Assess the morphology of the red blood cells.
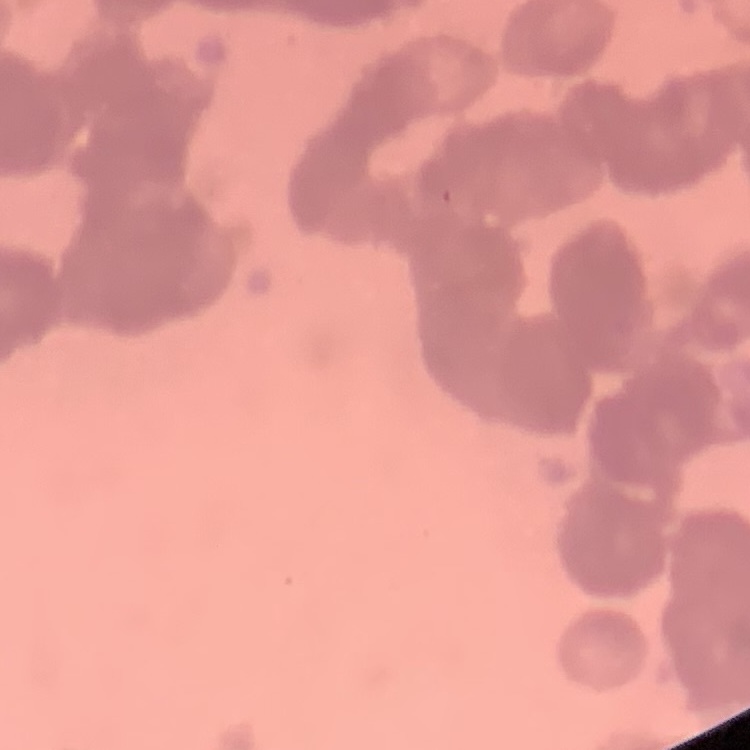
They show rouleaux formation.

Thin blood film. Stained with either Field's or Giemsa. Square crop of a larger photomicrograph.